Identify the parasite.
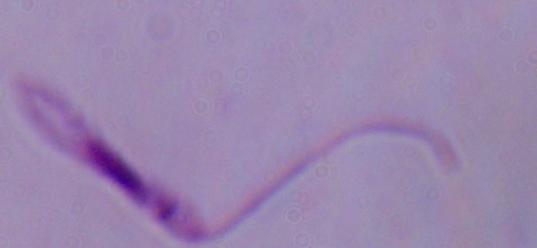

This is Leishmania.

Summary:
  - Magnification: 1000x
  - Modality: photomicrograph